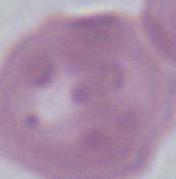
Summary:
  - Modality: micrograph
  - Magnification: 1000x
  - Identification: erythrocyte